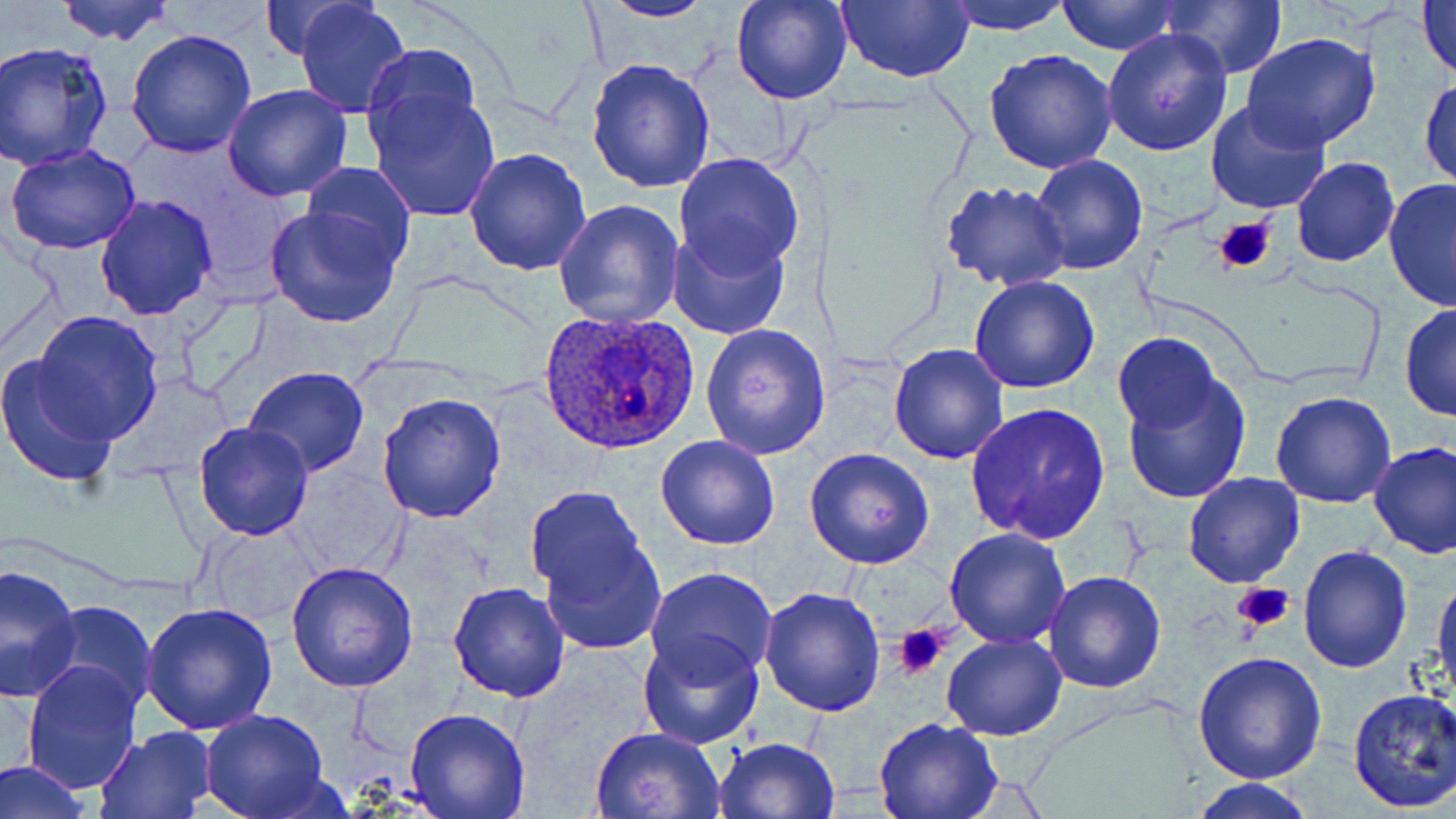

{
  "plasmodium_ovale_infected_red_blood_cell_locations": "approximate bounding boxes as (x1, y1, x2, y2) in pixels: (535, 308, 701, 456)",
  "slide_level_diagnosis": "Plasmodium ovale",
  "preparation": "thin blood film",
  "field_of_view": "one of a larger specimen",
  "platelet_locations": "approximate bounding boxes as (x1, y1, x2, y2) in pixels: (1214, 213, 1278, 276), (1231, 581, 1296, 634), (894, 623, 949, 677)",
  "stain": "May-Grünwald-Giemsa",
  "image_size": "1456×819 pixels",
  "magnification": "1000x",
  "uninfected_red_blood_cell_locations": "approximate bounding boxes as (x1, y1, x2, y2) in pixels: (54, 0, 177, 47), (257, 0, 361, 61), (293, 0, 411, 117), (731, 0, 854, 106), (837, 0, 972, 83), (943, 0, 1071, 34), (1056, 0, 1181, 54), (1418, 0, 1456, 83), (596, 1, 715, 23), (1164, 2, 1287, 78), (1104, 27, 1233, 155), (126, 29, 258, 158), (1242, 32, 1383, 151), (1, 41, 116, 173), (364, 42, 480, 146), (983, 49, 1118, 174), (585, 57, 716, 194), (1419, 74, 1455, 192), (222, 84, 353, 202), (367, 89, 501, 222), (1204, 100, 1332, 217), (4, 144, 144, 255), (464, 147, 592, 276), (674, 153, 804, 276), (1028, 154, 1147, 276), (1292, 157, 1399, 268), (301, 162, 416, 270), (1383, 176, 1456, 311), (938, 180, 1073, 291), (95, 193, 218, 320), (553, 198, 684, 330), (264, 203, 402, 328), (666, 227, 791, 339), (969, 275, 1099, 394), (1399, 304, 1455, 421), (34, 310, 162, 443), (701, 323, 831, 459), (1115, 331, 1222, 435), (888, 342, 1010, 463), (0, 354, 121, 487), (243, 367, 368, 477), (1122, 371, 1251, 504), (376, 390, 508, 523), (1270, 392, 1396, 510), (967, 402, 1112, 544), (193, 421, 314, 542), (654, 433, 781, 550), (1368, 441, 1456, 559), (804, 448, 934, 570), (283, 463, 411, 580), (1183, 472, 1305, 588), (525, 485, 649, 608), (198, 522, 326, 628), (943, 527, 1069, 648), (540, 534, 666, 655), (1298, 544, 1412, 673), (286, 561, 419, 691), (0, 563, 83, 703), (647, 567, 778, 680), (1043, 571, 1167, 694), (1432, 571, 1455, 704), (447, 581, 569, 701), (760, 585, 888, 717), (40, 601, 158, 714), (139, 604, 279, 736), (638, 630, 765, 749), (941, 632, 1067, 741), (1193, 650, 1328, 784), (19, 660, 143, 794), (1346, 687, 1456, 815), (403, 708, 530, 818), (200, 711, 331, 819), (872, 716, 1003, 819), (94, 724, 217, 817), (592, 726, 727, 819), (713, 736, 840, 819), (0, 758, 91, 819), (1188, 777, 1319, 818)",
  "modality": "light microscopy"
}